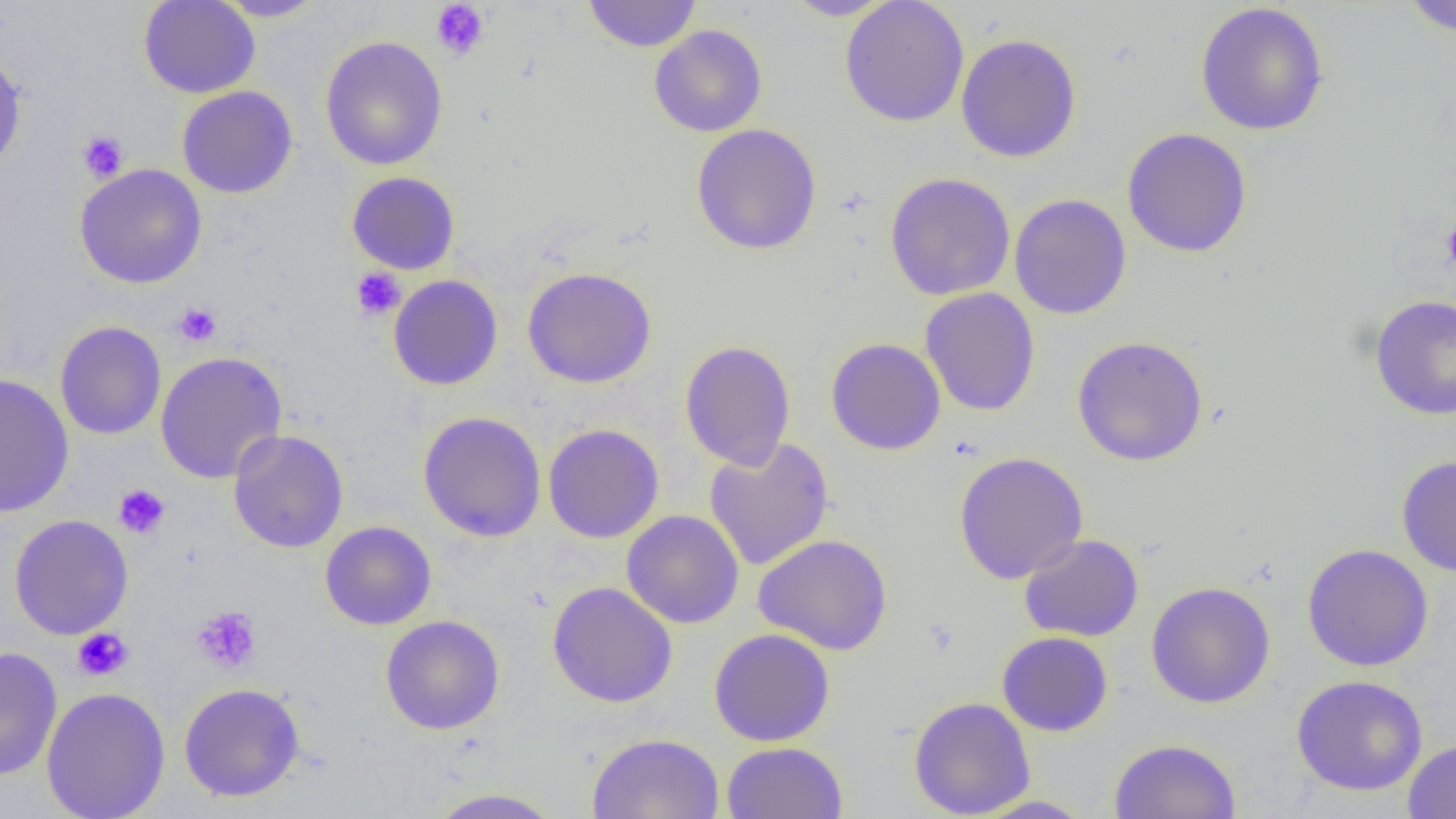

Approximate bounding boxes as (x1,y1)-(x2,y2) corner pairs in pixels. Uninfected red blood cell locations: (138,0)-(260,98), (214,0)-(329,22), (583,0)-(702,52), (783,0)-(896,20), (840,0)-(969,127), (1399,0)-(1456,37), (1194,2)-(1330,136), (649,24)-(767,137), (955,33)-(1082,163), (320,36)-(448,171), (0,46)-(27,174), (177,85)-(298,199), (691,123)-(822,255), (1121,127)-(1253,258), (75,163)-(207,289), (346,171)-(460,275), (884,172)-(1016,301), (1009,194)-(1132,320), (521,267)-(657,388), (388,274)-(503,391), (920,288)-(1041,417), (1369,295)-(1456,420), (54,321)-(166,440), (1071,335)-(1209,467), (826,337)-(946,456), (680,340)-(796,471), (154,350)-(288,484), (0,373)-(74,518), (418,411)-(547,542), (543,424)-(665,543), (228,429)-(348,553), (703,437)-(835,571), (953,451)-(1088,583), (1396,454)-(1456,577), (622,510)-(744,629), (9,514)-(133,640), (320,521)-(437,630), (753,533)-(893,655), (1019,533)-(1144,642), (1301,543)-(1434,672), (547,581)-(678,708), (1145,581)-(1276,709), (380,615)-(505,734), (708,628)-(836,746), (997,632)-(1113,736), (0,646)-(63,781), (1291,675)-(1428,796), (178,683)-(305,802), (41,687)-(170,819), (909,696)-(1036,818), (586,732)-(725,819), (1108,738)-(1242,819), (1403,738)-(1456,819), (721,741)-(848,818), (424,788)-(565,818), (969,795)-(1096,818). Platelet locations: (430,0)-(490,60), (77,130)-(129,183), (1440,216)-(1456,278), (351,267)-(406,320), (172,302)-(222,347), (113,484)-(170,539), (191,605)-(262,674), (72,628)-(133,682). Slide-level diagnosis: negative for blood parasites. Optical microscopy. Image is 1456×819 pixels. Thin blood smear. Single field of view. 1000x magnification.